Classify this cell by malaria status.
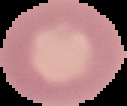
Uninfected.

image type = segmented cell region with the area outside set to black
preparation = thin blood film
image size = 127×106 pixels